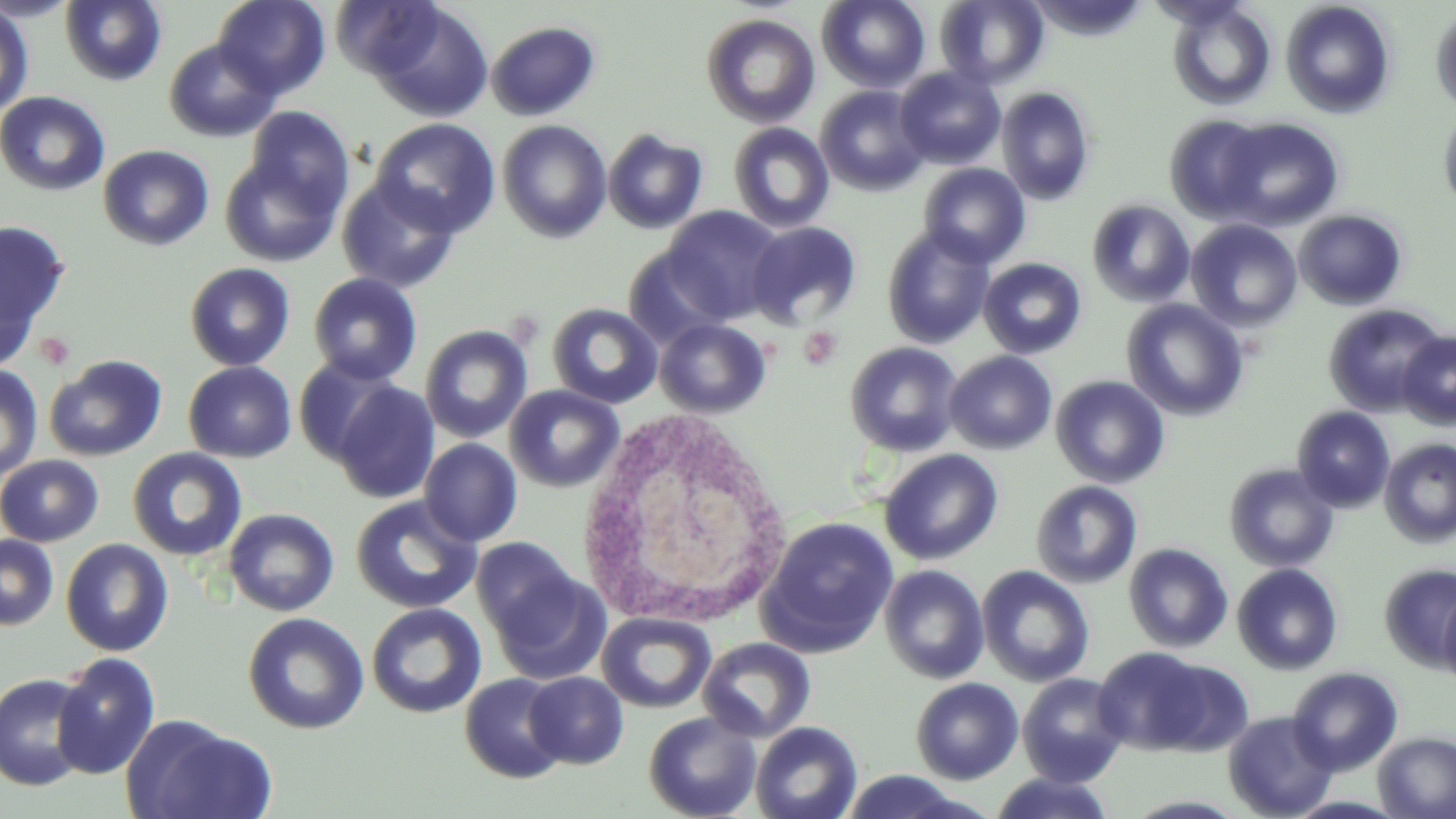

slide-level diagnosis = negative for blood parasites
preparation = thin blood smear
field of view = one of a larger specimen
uninfected red blood cell locations = approximate bounding boxes as (x1,y1)-(x2,y2) corner pairs in pixels: (0,0)-(82,22), (59,0)-(166,86), (213,0)-(330,99), (329,0)-(443,78), (817,0)-(931,93), (935,1)-(1049,89), (1166,1)-(1276,111), (1280,1)-(1396,119), (372,3)-(494,123), (0,4)-(34,118), (1430,6)-(1456,114), (701,13)-(821,129), (486,21)-(601,121), (163,38)-(280,143), (894,66)-(1006,169), (815,85)-(931,196), (996,86)-(1095,205), (0,91)-(110,196), (242,106)-(356,220), (1439,108)-(1456,215), (1164,115)-(1270,222), (1218,117)-(1344,231), (371,118)-(501,237), (497,120)-(612,243), (728,122)-(835,233), (602,128)-(709,235), (98,144)-(215,251), (220,152)-(344,267), (919,163)-(1031,268), (338,177)-(461,293), (325,178)-(440,385), (1087,199)-(1195,308), (661,206)-(786,324), (1294,209)-(1408,311), (1186,219)-(1302,331), (0,220)-(70,357), (746,221)-(862,328), (882,226)-(995,349), (622,248)-(732,348), (979,257)-(1087,359), (185,262)-(295,371), (308,273)-(423,385), (1121,299)-(1248,421), (546,303)-(663,409), (1323,303)-(1448,416), (654,317)-(773,419), (420,324)-(533,443), (1396,331)-(1456,429), (845,342)-(963,456), (944,351)-(1057,455), (44,354)-(168,461), (293,356)-(402,467), (183,361)-(297,463), (0,364)-(44,481), (1050,375)-(1170,489), (332,381)-(441,505), (504,384)-(624,493), (1292,406)-(1396,513), (419,438)-(522,547), (1379,438)-(1456,548), (127,447)-(248,562), (879,448)-(1004,566), (0,455)-(104,547), (1224,463)-(1339,572), (1031,480)-(1143,588), (351,495)-(482,615), (224,508)-(339,616), (759,516)-(898,656), (0,534)-(59,631), (60,538)-(173,656), (471,538)-(583,644), (1124,543)-(1233,653), (1380,563)-(1456,670), (486,564)-(610,684), (879,564)-(990,684), (1232,564)-(1343,675), (976,565)-(1094,687), (1439,589)-(1456,692), (366,603)-(486,718), (598,611)-(716,713), (243,613)-(369,735), (698,637)-(816,743), (1093,646)-(1223,755), (51,652)-(161,779), (1287,667)-(1404,776), (0,672)-(94,791), (523,672)-(629,769), (459,673)-(570,784), (1016,673)-(1130,787), (911,678)-(1024,784), (1222,710)-(1339,819), (644,712)-(761,819), (122,715)-(274,819), (751,721)-(863,819), (1373,732)-(1456,818), (838,770)-(983,819), (988,772)-(1115,819), (1281,795)-(1411,818)
image size = 1456×819 pixels
modality = optical microscopy
magnification = 1000x
white blood cell locations = approximate bounding boxes as (x1,y1)-(x2,y2) corner pairs in pixels: (576,410)-(796,629)
stain = May-Grünwald-Giemsa
platelet locations = approximate bounding boxes as (x1,y1)-(x2,y2) corner pairs in pixels: (799,327)-(844,369), (34,331)-(76,370)